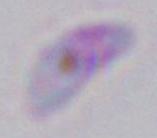

Summary:
  - Modality: photomicrograph
  - Identification: Toxoplasma gondii
  - Magnification: 1000x